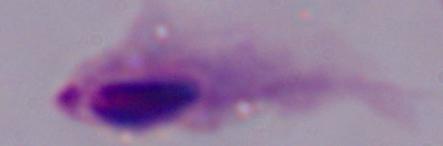 A trichomonad is seen. Photomicrograph. 1000x magnification.